Report the malaria status of this cell.
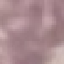

Uninfected.

Photographed with a smartphone camera at the microscope eyepiece. Cell patch, automatically extracted from a larger field of view and resized to 64 × 64 pixels. Thin smear of blood. Giemsa-stained preparation.